Name the parasite shown.
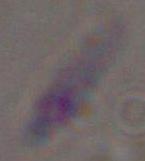

This is Toxoplasma gondii.

modality = photomicrograph
magnification = 1000x